State the preparation type.
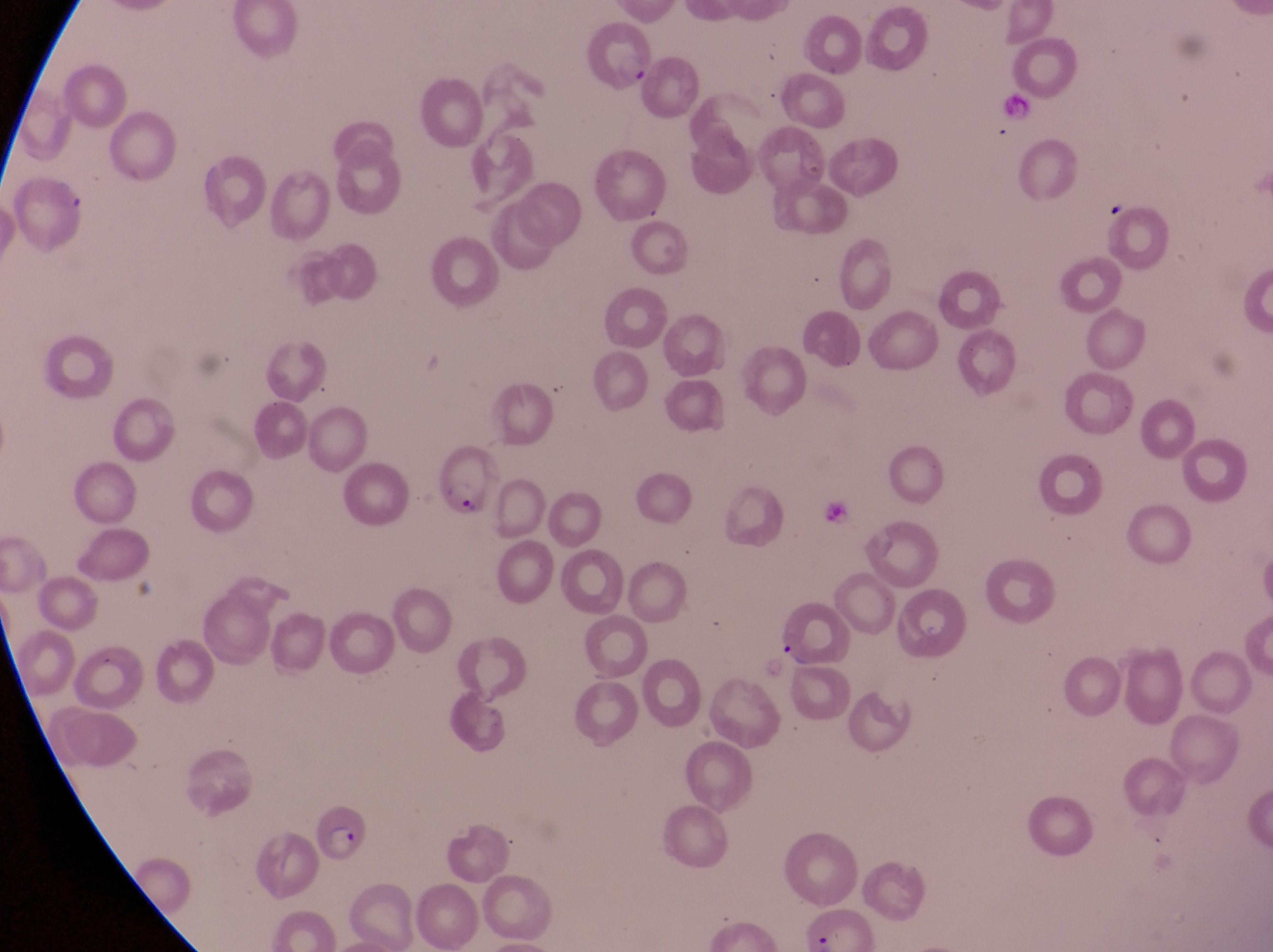

This is a thin smear.

Approximate bounding boxes as (left, top, right, bottom) in pixels. Parasitised red blood cell locations: (582, 23, 659, 95), (427, 447, 499, 515), (307, 797, 369, 865). Artifact (platelet-like body, stain precipitate, or debris) locations: (1103, 195, 1131, 222). Collected in Uganda. Magnification of 1000x. Single field of view. Photographed through the eyepiece of an Olympus CX-23 microscope with a smartphone camera. Image is 1273×952 pixels.